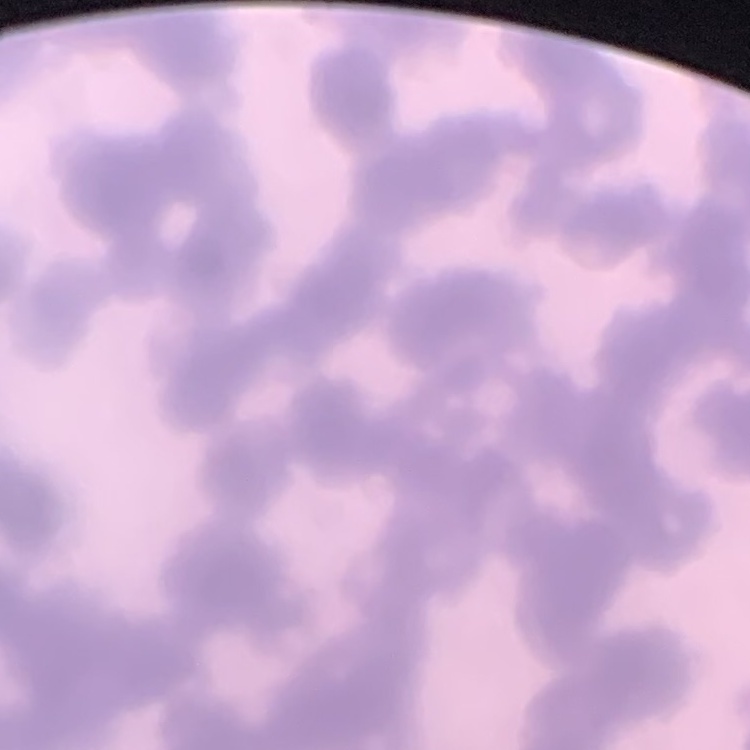

The erythrocytes exhibit rouleaux formation. Square crop of a larger photomicrograph. Field's or Giemsa stain. Thin blood smear.